Report the malaria status of this cell.
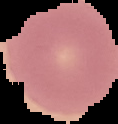

It is uninfected.

Image is 118×124 pixels. From a thin blood film. Segmented cell region on a black background.